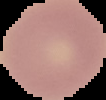
preparation: thin blood smear
image_size: 106×100 pixels
image_type: cell region segmented out of the field of view; surrounding area masked to black
result: no Plasmodium parasites seen